Assess the morphology of the red blood cells.
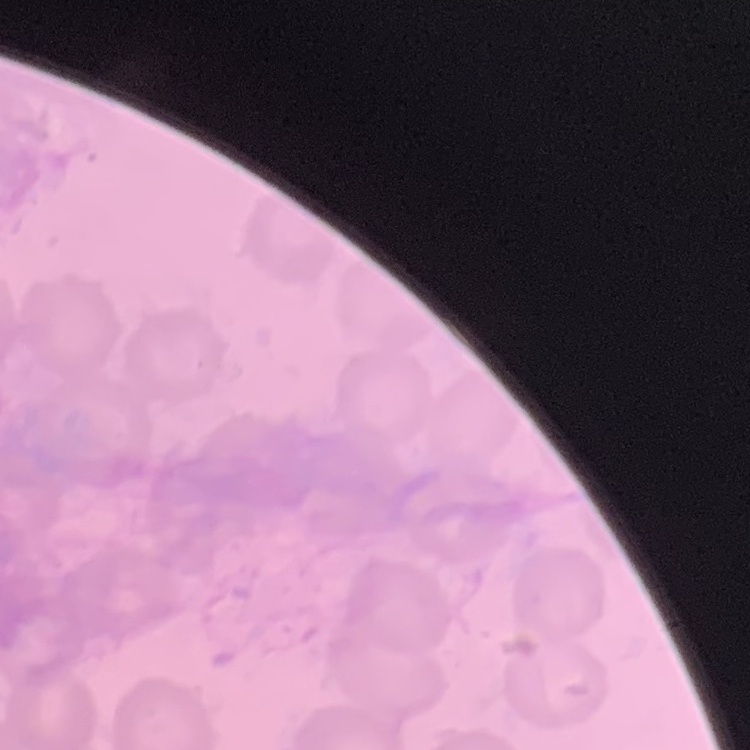
No rouleaux formation.

Stained with either Field's or Giemsa. One tile cut from a larger photomicrograph. Thin blood film.